Report the malaria status.
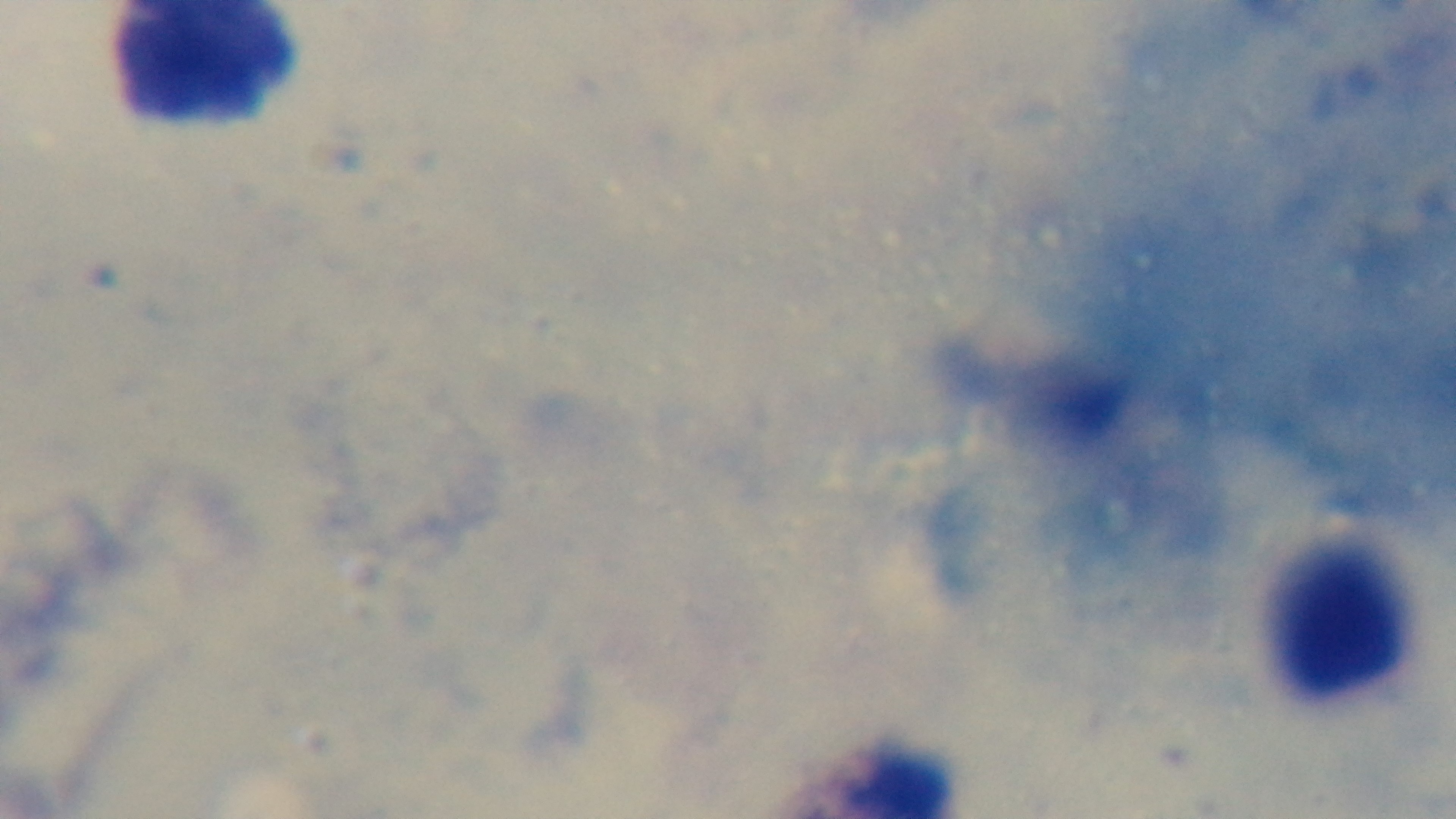
Negative.

Giemsa stain. Light microscopy. Mounted 4K digital camera. Preparation: thick smear. Oil-immersion objective, 100x. Single field of view.